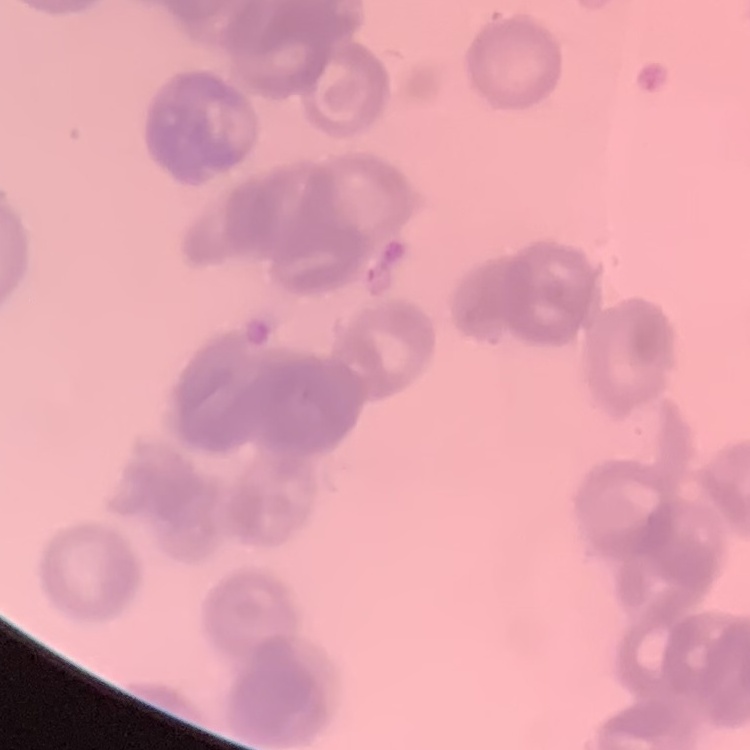
erythrocyte morphology = rouleaux formation
stain = Field's or Giemsa
image type = square crop of a larger photomicrograph
preparation = thin blood smear